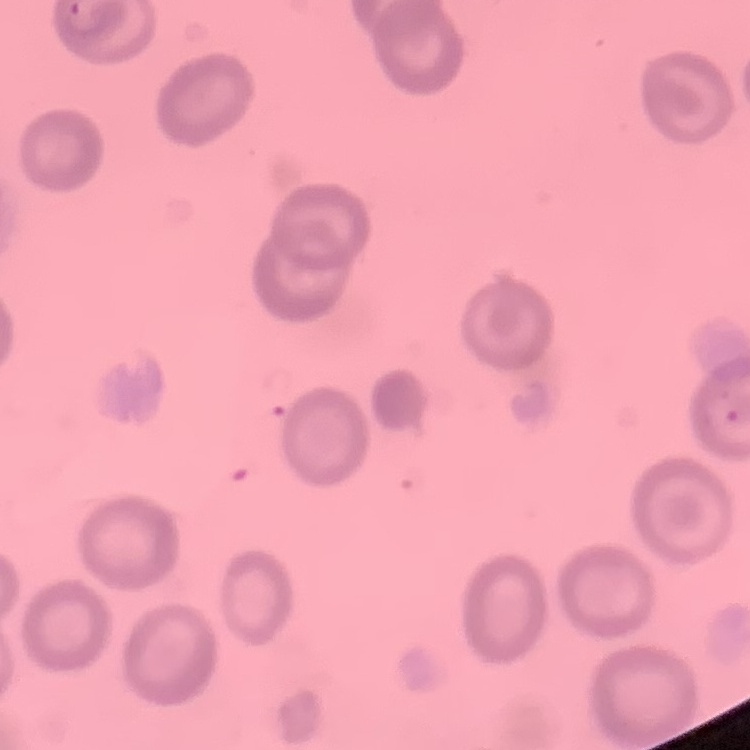

The red blood cells exhibit no rouleaux formation. Field's or Giemsa stain. Thin peripheral smear. One tile cut from a larger photomicrograph.